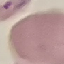

Summary:
  - Malaria status: parasitized
  - Stain: Giemsa
  - Capture: smartphone camera at the microscope eyepiece
  - Image type: automatically extracted cell patch, resized to 64 × 64 pixels
  - Preparation: thin smear